Assess this cell for malaria.
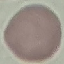

It is uninfected.

Summary:
  - Capture: smartphone through the microscope eyepiece
  - Preparation: thin blood film
  - Stain: Giemsa
  - Image type: cell patch, automatically extracted from a larger field of view and resized to 64 × 64 pixels